Locate malaria parasites and leukocytes.
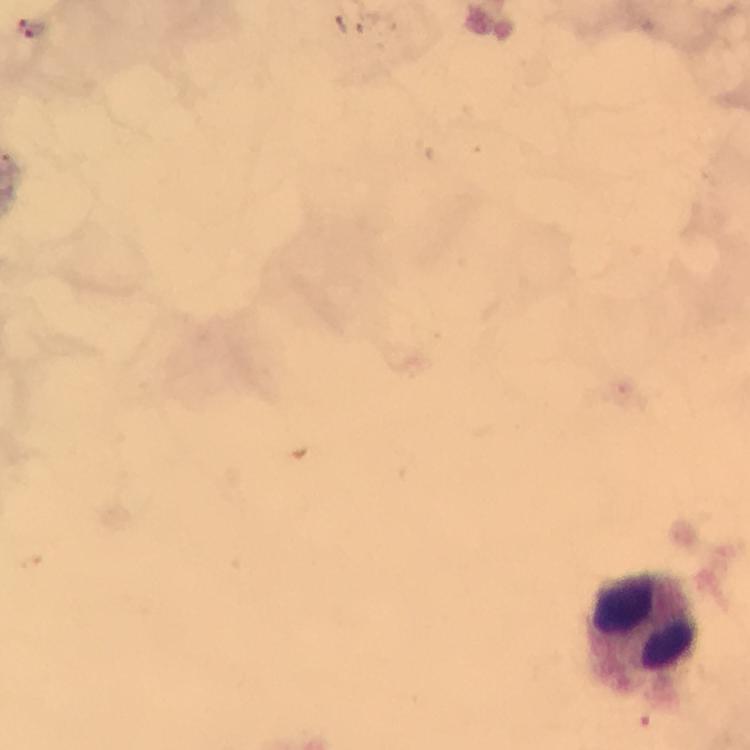
Approximate object centers, in pixels from the top-left corner.
Malaria parasites: (x=36, y=33).
Leukocytes: (x=640, y=639).

Summary:
  - Image size: 750×750 pixels
  - Magnification: 100x
  - Stain: Giemsa
  - Immersion oil: applied
  - Cropped from: one field of view
  - Context: from a malaria diagnostic workup
  - Capture: smartphone photograph through a microscope
  - Preparation: thick blood film